Assess the morphology of the erythrocytes.
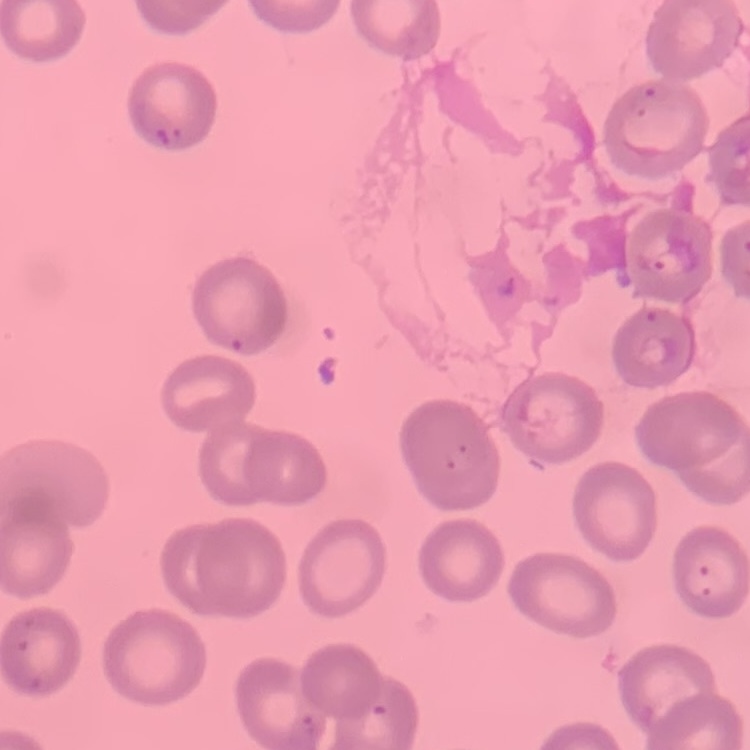

No rouleaux formation.

preparation = thin peripheral smear
stain = Field's or Giemsa
image type = square crop of a larger photomicrograph